Name the parasite shown.
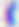

Toxoplasma gondii.

magnification = 400x
modality = micrograph